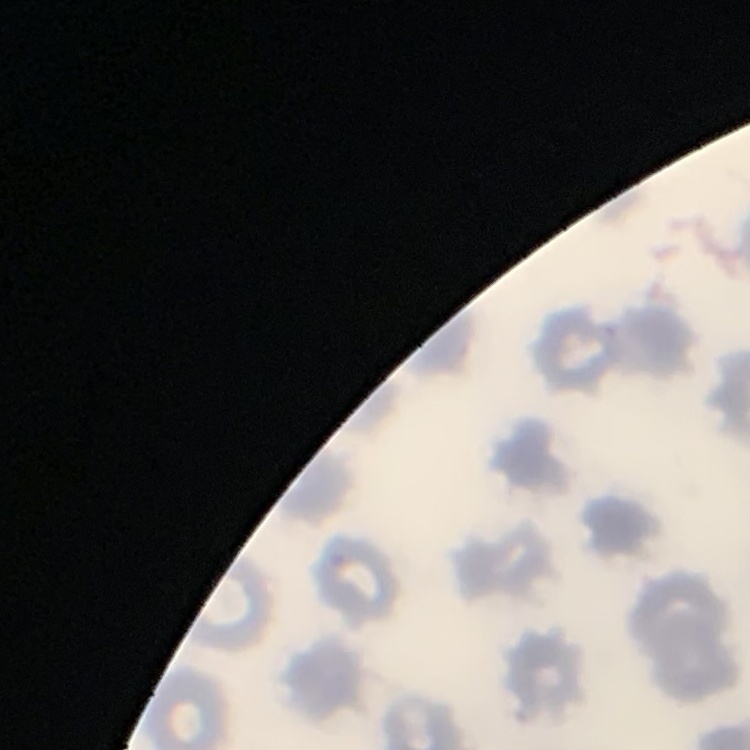
Summary:
  - Erythrocyte morphology: no rouleaux formation
  - Stain: Field's or Giemsa
  - Image type: square crop of a larger photomicrograph
  - Preparation: thin peripheral smear